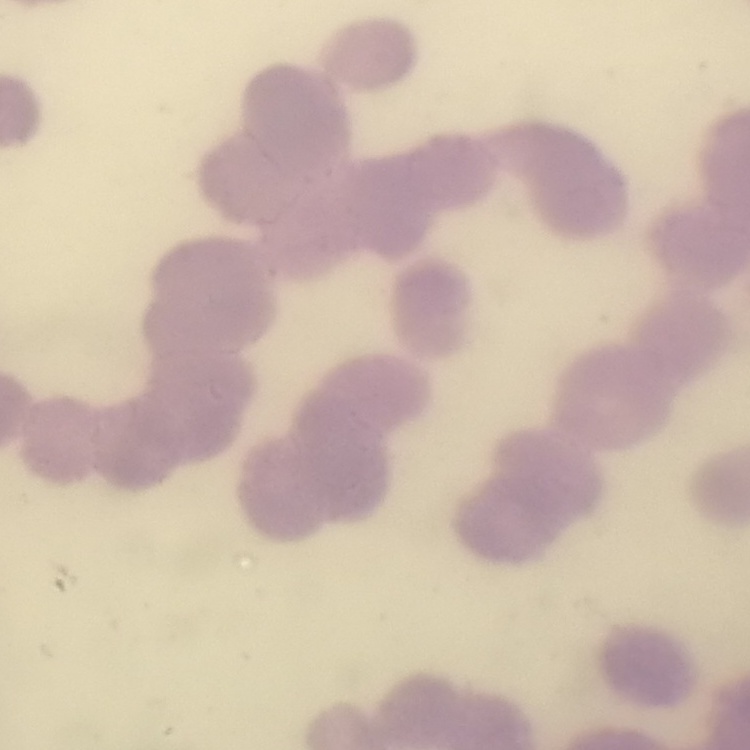

Summary:
  - Erythrocyte morphology: rouleaux formation
  - Image type: square crop of a larger photomicrograph
  - Preparation: thin blood film
  - Stain: Field's or Giemsa